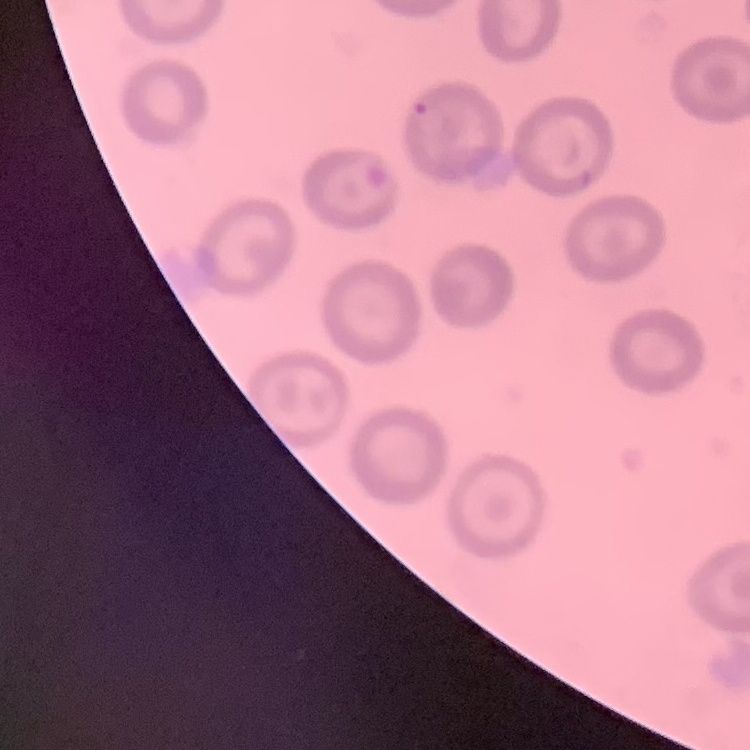

{
  "red_blood_cell_morphology": "no rouleaux formation",
  "preparation": "thin blood film",
  "stain": "Field's or Giemsa",
  "image_type": "one tile cut from a larger photomicrograph"
}